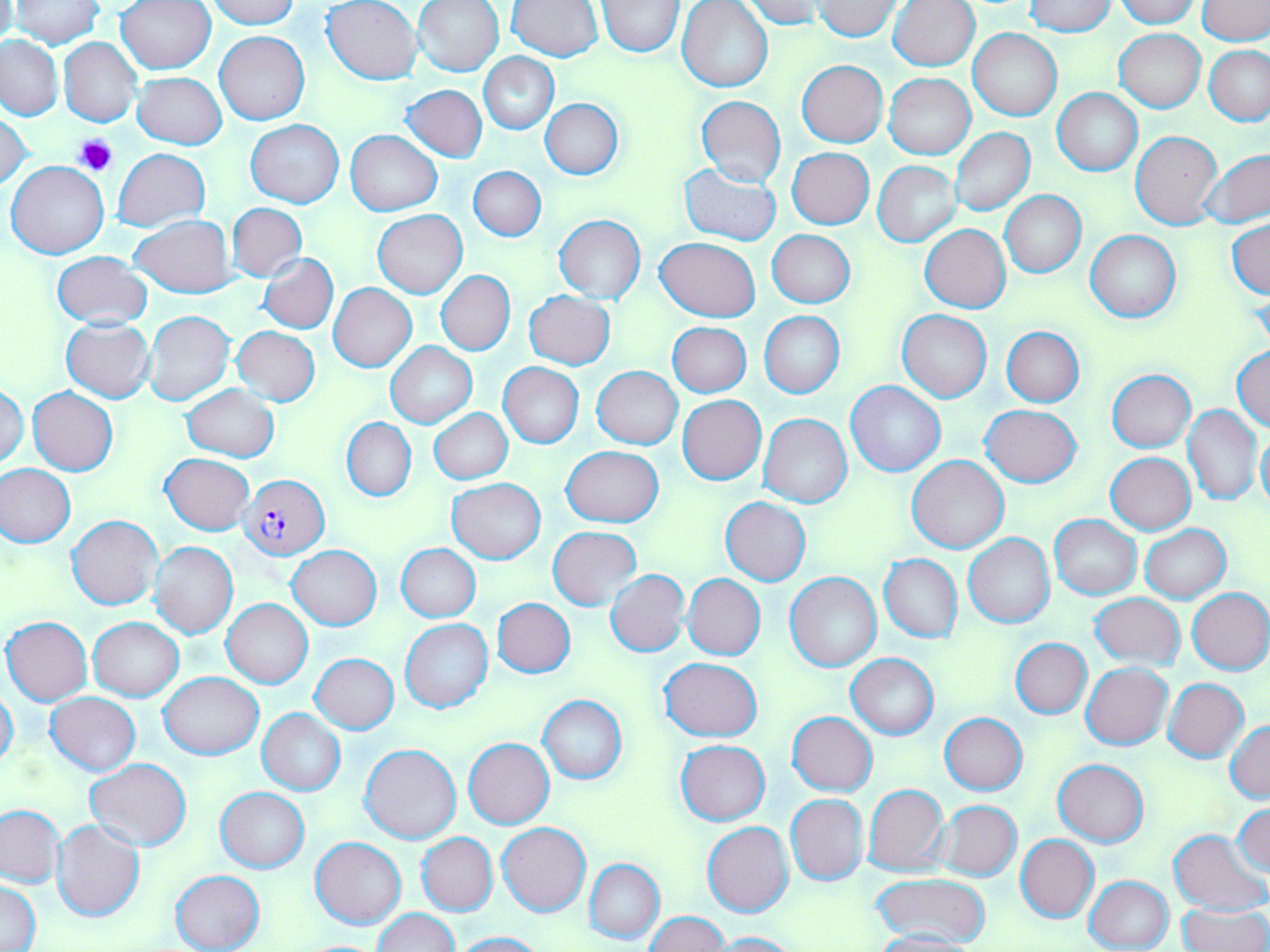

Approximate bounding boxes as [x1, y1, x2, y2] in pixels. Platelet locations: [76, 135, 117, 177]. Plasmodium falciparum-infected red blood cell locations: [241, 473, 330, 560]. Uninfected red blood cell locations: [0, 0, 18, 48], [116, 0, 216, 74], [207, 0, 299, 28], [413, 0, 504, 76], [740, 0, 824, 28], [1114, 0, 1198, 27], [10, 1, 102, 49], [322, 1, 422, 85], [507, 1, 604, 61], [598, 1, 683, 56], [677, 1, 773, 92], [814, 1, 903, 40], [890, 1, 979, 70], [1024, 1, 1116, 36], [1196, 1, 1268, 46], [968, 28, 1061, 121], [1114, 28, 1206, 112], [214, 31, 309, 124], [0, 36, 64, 119], [59, 38, 142, 127], [1205, 45, 1270, 126], [479, 54, 557, 133], [796, 60, 888, 147], [132, 71, 226, 150], [884, 74, 975, 159], [403, 85, 488, 162], [1053, 88, 1143, 176], [695, 96, 786, 187], [540, 98, 624, 179], [1, 110, 32, 193], [246, 120, 344, 208], [950, 128, 1035, 216], [345, 130, 441, 215], [1131, 130, 1223, 230], [787, 148, 873, 228], [113, 149, 209, 231], [1200, 151, 1270, 229], [7, 161, 110, 259], [873, 161, 960, 246], [679, 163, 782, 246], [469, 166, 545, 241], [1000, 190, 1086, 277], [227, 203, 306, 282], [373, 210, 467, 298], [553, 214, 646, 303], [130, 216, 236, 297], [1227, 219, 1270, 299], [920, 224, 1010, 313], [767, 229, 855, 308], [1086, 230, 1180, 322], [656, 237, 759, 321], [51, 250, 153, 329], [259, 254, 338, 334], [436, 270, 515, 356], [329, 283, 416, 373], [525, 290, 615, 369], [897, 310, 991, 402], [145, 311, 235, 407], [759, 311, 844, 398], [61, 318, 156, 404], [667, 322, 752, 397], [232, 325, 319, 406], [1002, 328, 1084, 407], [386, 341, 477, 428], [1231, 344, 1270, 432], [498, 362, 584, 448], [592, 366, 683, 450], [1107, 370, 1195, 451], [845, 381, 945, 476], [0, 383, 28, 468], [182, 385, 278, 461], [28, 388, 118, 476], [677, 395, 766, 485], [1182, 403, 1261, 507], [981, 404, 1081, 486], [430, 409, 512, 484], [758, 413, 851, 507], [342, 418, 415, 501], [1257, 428, 1270, 515], [560, 446, 664, 526], [1105, 452, 1196, 533], [161, 453, 253, 534], [907, 455, 1009, 553], [0, 464, 75, 547], [447, 479, 546, 563], [720, 497, 810, 585], [1049, 514, 1141, 599], [68, 515, 162, 610], [1140, 525, 1230, 602], [548, 527, 641, 610], [963, 532, 1054, 628], [152, 542, 238, 639], [396, 544, 480, 622], [288, 545, 381, 629], [879, 554, 962, 643], [605, 569, 689, 658], [784, 573, 881, 672], [684, 574, 765, 660], [1187, 588, 1270, 675], [1089, 594, 1185, 668], [492, 598, 575, 677], [222, 599, 312, 688], [2, 617, 92, 706], [89, 617, 183, 701], [400, 619, 492, 713], [1011, 638, 1092, 718], [311, 653, 398, 733], [847, 654, 938, 738], [659, 657, 762, 740], [1081, 663, 1174, 750], [159, 672, 263, 760], [1163, 678, 1248, 762], [0, 685, 19, 771], [45, 692, 141, 775], [538, 695, 627, 785], [257, 709, 346, 795], [788, 712, 877, 795], [939, 713, 1028, 795], [1225, 721, 1269, 803], [463, 738, 555, 829], [675, 740, 771, 825], [359, 742, 462, 845], [85, 757, 191, 851], [1053, 759, 1148, 846], [863, 784, 948, 876], [216, 787, 309, 872], [785, 794, 868, 886], [934, 801, 1021, 881], [1232, 802, 1269, 877], [0, 803, 65, 888], [51, 820, 145, 923], [703, 821, 794, 917], [497, 822, 590, 916], [1168, 829, 1267, 915], [417, 833, 498, 916], [1017, 834, 1098, 922], [311, 836, 405, 927], [585, 858, 664, 944], [170, 870, 265, 952], [871, 872, 990, 945], [1085, 875, 1175, 952], [0, 879, 40, 952], [1176, 902, 1269, 952], [374, 908, 457, 951], [645, 912, 728, 951], [871, 930, 980, 952], [452, 931, 549, 951], [707, 931, 804, 951]. Slide-level diagnosis: Plasmodium falciparum. 1000x magnification. Image is 1270×952 pixels. Thin blood film. Single field of view. Optical microscopy. May-Grünwald-Giemsa-stained preparation.